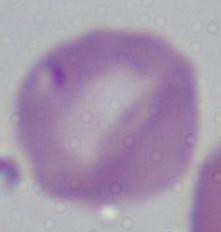

Summary:
  - Magnification: 1000x
  - Modality: photomicrograph
  - Identification: Babesia